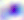
identification: Toxoplasma gondii
modality: micrograph
magnification: 400x